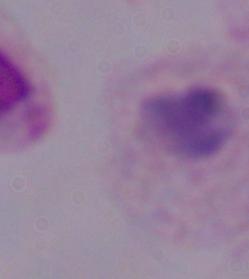
Summary:
  - Modality: micrograph
  - Magnification: 1000x
  - Identification: trichomonad